Locate and identify every blood parasite.
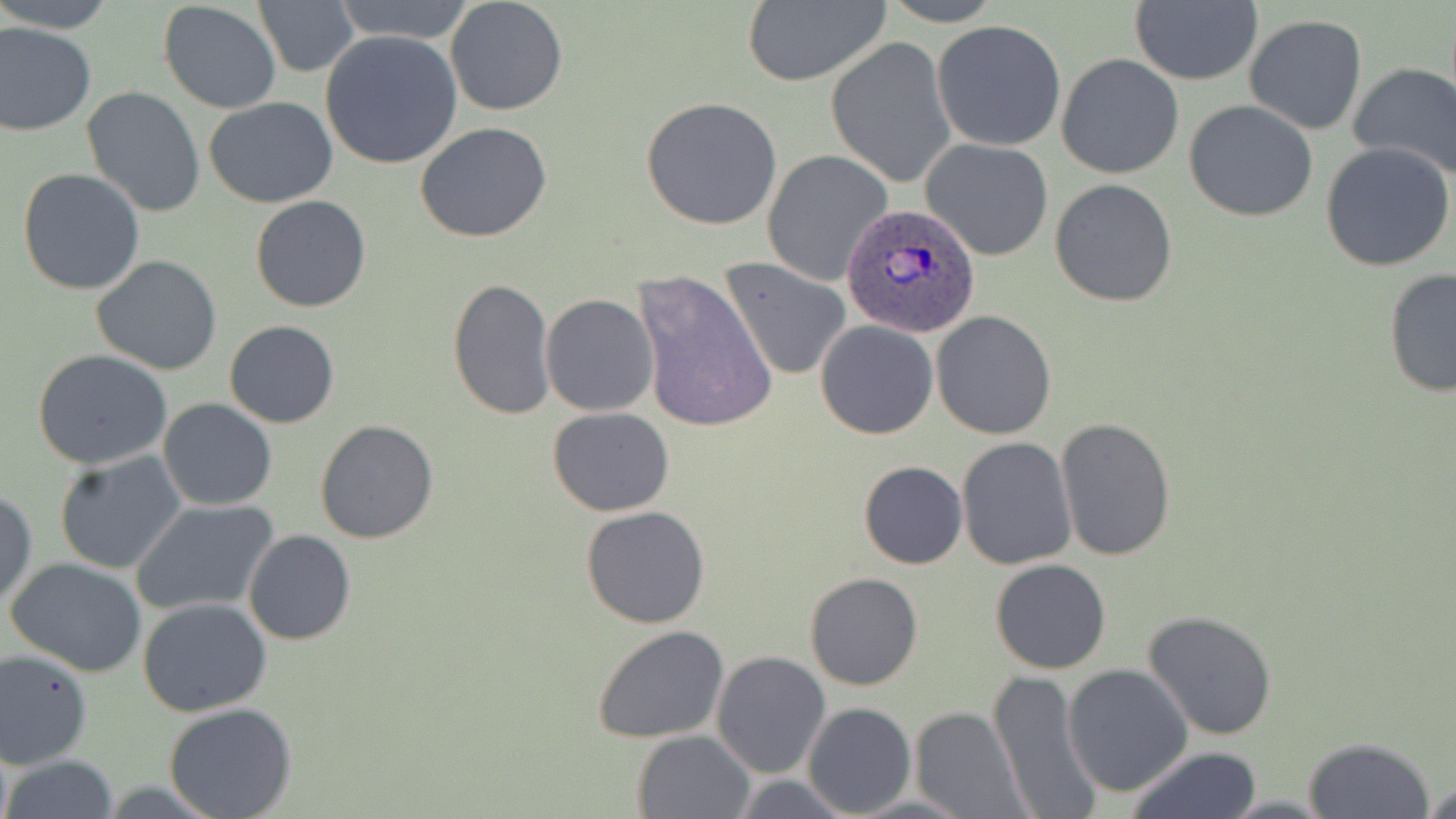

Approximate bounding boxes as [x1, y1, x2, y2] in pixels.
Plasmodium ovale-infected red blood cells: [844, 202, 980, 339].
No Plasmodium falciparum, Plasmodium malariae, Plasmodium vivax, Babesia divergens, or Trypanosoma brucei observed.

slide-level diagnosis = Plasmodium ovale
image size = 1456×819 pixels
modality = light microscopy
field of view = one of a larger specimen
preparation = thin blood smear
magnification = 1000x
stain = May-Grünwald-Giemsa
uninfected red blood cell locations = approximate bounding boxes as [x1, y1, x2, y2] in pixels: [4, 0, 114, 32], [331, 0, 477, 45], [444, 0, 569, 117], [880, 0, 1007, 26], [1129, 0, 1261, 86], [158, 2, 282, 114], [254, 2, 359, 76], [740, 2, 890, 86], [1243, 15, 1367, 136], [933, 20, 1065, 151], [0, 23, 96, 135], [319, 30, 462, 170], [827, 35, 956, 190], [3, 45, 126, 188], [1056, 53, 1184, 178], [1348, 62, 1456, 184], [80, 85, 206, 219], [640, 95, 784, 231], [203, 97, 338, 208], [1184, 100, 1318, 221], [415, 122, 552, 243], [921, 139, 1055, 261], [1321, 142, 1455, 271], [762, 149, 892, 287], [17, 169, 146, 296], [1050, 179, 1179, 308], [250, 195, 373, 313], [91, 255, 222, 374], [721, 256, 850, 381], [1382, 268, 1456, 397], [631, 270, 777, 433], [448, 278, 557, 420], [541, 294, 659, 417], [931, 310, 1057, 440], [224, 319, 340, 428], [815, 319, 938, 439], [32, 350, 174, 470], [158, 399, 277, 511], [548, 406, 675, 516], [1055, 417, 1177, 562], [314, 419, 440, 542], [956, 437, 1077, 570], [53, 451, 188, 574], [859, 461, 968, 569], [0, 486, 37, 612], [131, 499, 279, 617], [581, 506, 711, 629], [242, 529, 357, 645], [6, 558, 148, 677], [990, 559, 1110, 675], [806, 572, 924, 691], [139, 597, 272, 717], [1143, 609, 1279, 742], [594, 626, 731, 744], [0, 649, 94, 768], [712, 651, 830, 777], [1062, 664, 1193, 798], [988, 671, 1104, 818], [163, 702, 298, 819], [803, 702, 915, 817], [910, 708, 1027, 817], [631, 729, 754, 818], [1301, 737, 1434, 819], [1124, 746, 1264, 819], [2, 756, 119, 819], [729, 775, 853, 817], [1423, 779, 1455, 817], [843, 793, 974, 817]